State which parasite is depicted.
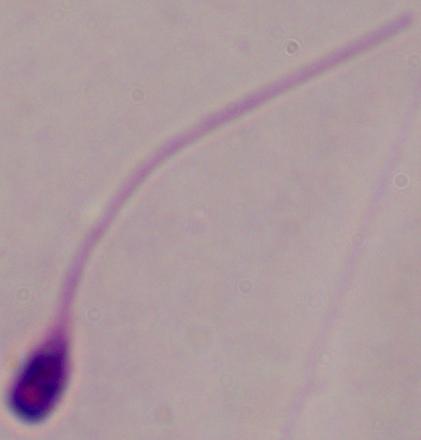
This is Leishmania.

Summary:
  - Magnification: 1000x
  - Modality: photomicrograph